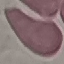

Summary:
  - Malaria status: uninfected
  - Preparation: thin blood film
  - Stain: Giemsa
  - Capture: smartphone camera at the microscope eyepiece
  - Image type: automatically extracted cell patch, resized to 64 × 64 pixels